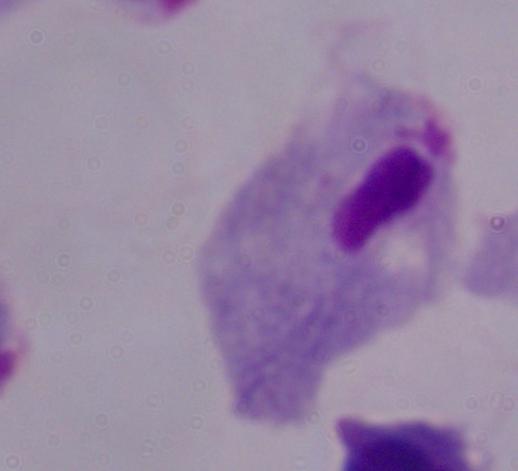 Micrograph. A trichomonad is shown. Captured at 1000x magnification.